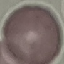
Summary:
  - Malaria status: uninfected
  - Stain: Giemsa
  - Capture: smartphone through the microscope eyepiece
  - Image type: automatically extracted cell patch, resized to 64 × 64 pixels
  - Preparation: thin blood film